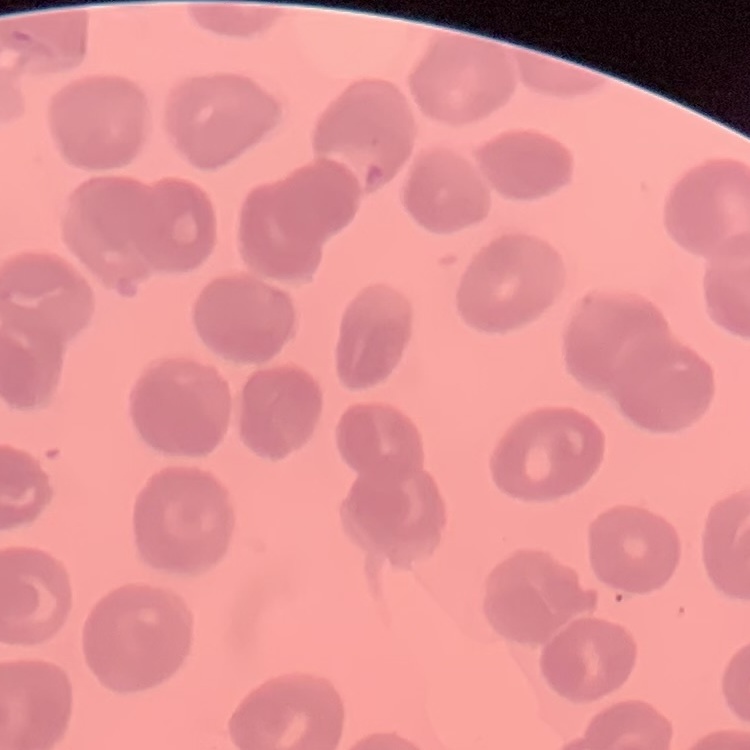

Summary:
  - Erythrocyte morphology: no rouleaux formation
  - Image type: one tile cut from a larger photomicrograph
  - Preparation: thin blood smear
  - Stain: Field's or Giemsa